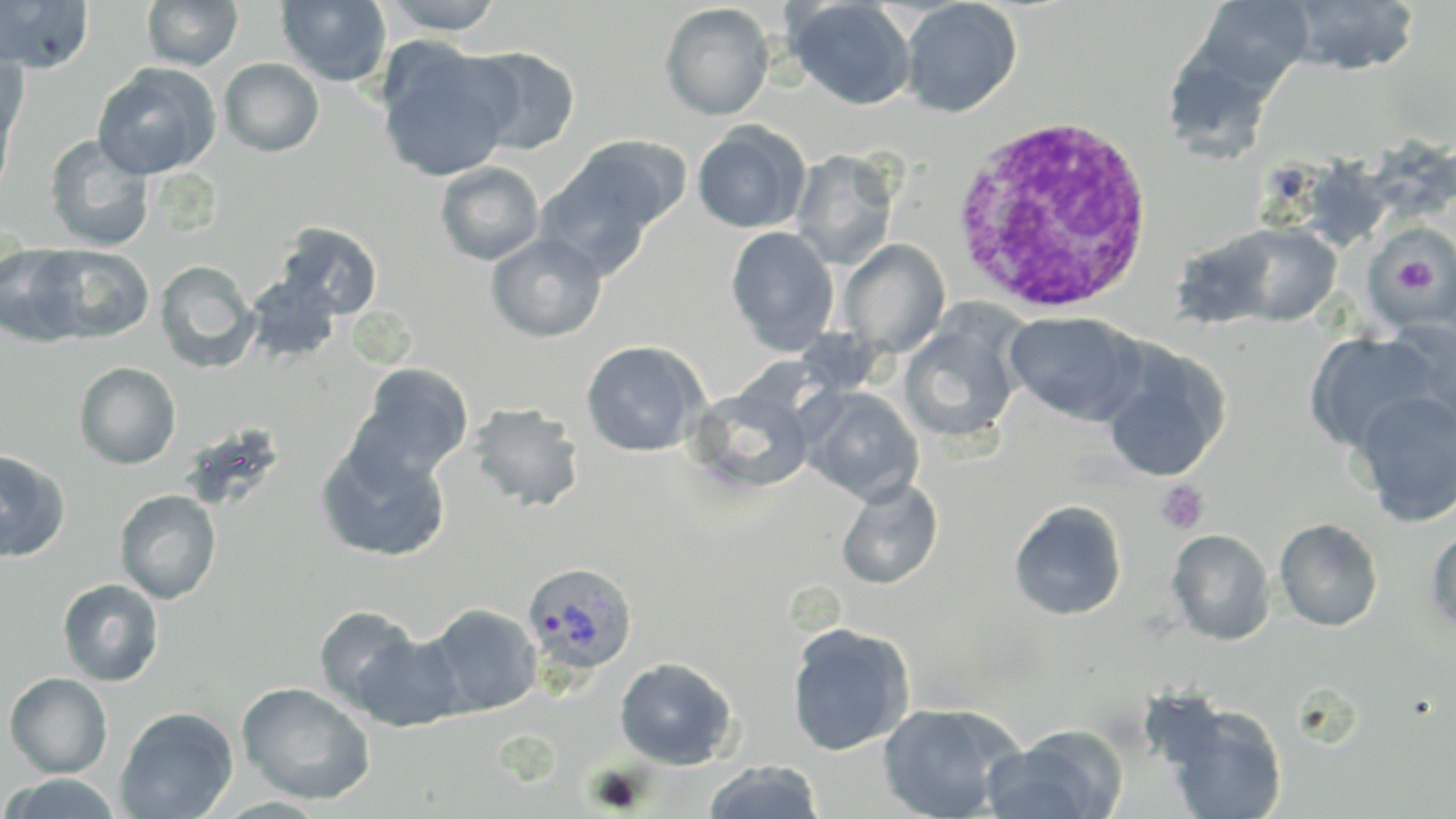
Approximate bounding boxes as (x1,y1)-(x2,y2) corner pairs in pixels. White blood cell locations: (947,116)-(1158,314). Uninfected red blood cell locations: (0,0)-(96,73), (141,0)-(243,70), (276,0)-(392,87), (379,0)-(508,35), (785,0)-(917,111), (1195,0)-(1314,93), (1282,0)-(1421,75), (900,1)-(1022,117), (660,3)-(775,121), (377,40)-(516,183), (0,46)-(30,145), (462,46)-(581,155), (219,58)-(324,156), (91,62)-(221,181), (0,98)-(15,205), (692,123)-(810,234), (44,134)-(154,251), (538,144)-(675,275), (791,148)-(900,270), (435,162)-(544,265), (278,222)-(384,319), (1218,223)-(1343,325), (1366,225)-(1456,327), (725,226)-(839,356), (1170,230)-(1286,329), (486,232)-(607,343), (839,239)-(950,357), (0,242)-(96,346), (38,244)-(155,344), (155,260)-(259,372), (245,273)-(342,364), (1004,311)-(1143,425), (897,316)-(1023,446), (1304,330)-(1443,454), (580,340)-(708,457), (1096,340)-(1230,483), (75,361)-(181,469), (352,364)-(472,483), (688,385)-(814,495), (800,386)-(924,504), (1352,388)-(1456,526), (468,402)-(585,512), (316,438)-(452,563), (0,450)-(70,563), (836,477)-(943,590), (115,489)-(222,603), (1008,499)-(1127,621), (1274,517)-(1384,631), (1167,528)-(1276,645), (1427,529)-(1456,637), (58,578)-(164,686), (421,603)-(543,718), (314,604)-(423,712), (785,621)-(915,755), (352,629)-(466,731), (614,656)-(738,769), (4,671)-(113,778), (237,681)-(376,804), (877,701)-(1022,819), (1164,702)-(1288,818), (115,707)-(238,818), (983,728)-(1125,819), (702,760)-(825,818), (0,774)-(126,818). Plasmodium ovale-infected red blood cell locations: (523,561)-(638,675). Platelet locations: (1397,258)-(1437,297), (1156,482)-(1209,534). Slide-level diagnosis: Plasmodium ovale. Image is 1456×819 pixels. 1000x magnification. May-Grünwald-Giemsa stain. Light microscopy. Single field of view. Thin blood smear.